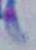

magnification: 1000x
modality: micrograph
identification: Toxoplasma gondii